State which parasite is depicted.
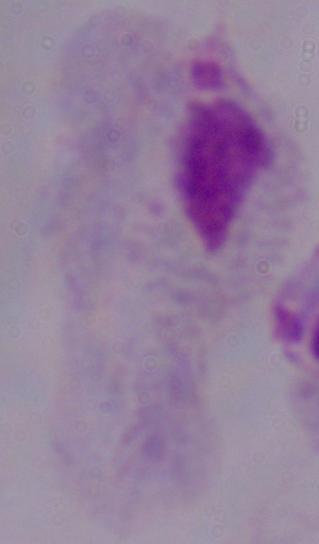
This is a trichomonad.

Summary:
  - Magnification: 1000x
  - Modality: photomicrograph